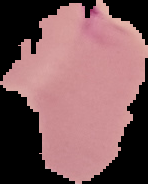

Summary:
  - Result: malaria parasites detected
  - Preparation: thin blood smear
  - Image type: segmented cell region with the area outside set to black
  - Image size: 148×184 pixels